Locate every blood parasite and identify its species.
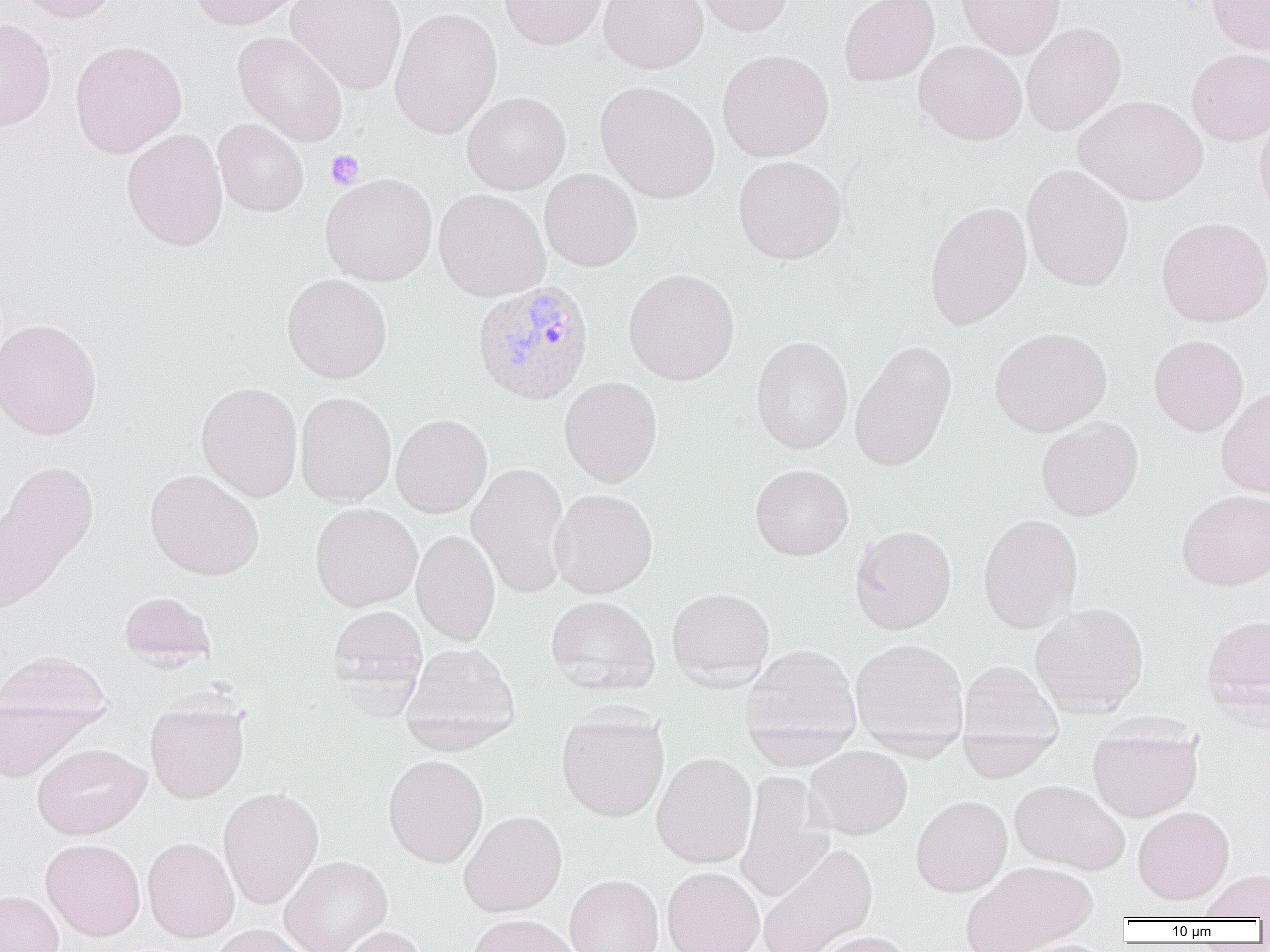

Approximate bounding boxes as [x1, y1, x2, y2] in pixels.
Plasmodium vivax-infected red blood cells: [472, 280, 594, 405].
No Plasmodium falciparum, Plasmodium ovale, Plasmodium malariae, Babesia divergens, or Trypanosoma brucei observed.

slide-level diagnosis = Plasmodium vivax
field of view = single
uninfected red blood cell locations = approximate bounding boxes as [x1, y1, x2, y2] in pixels: [10, 0, 121, 23], [188, 0, 305, 31], [286, 0, 407, 94], [498, 0, 608, 50], [598, 0, 708, 73], [692, 0, 795, 36], [839, 0, 939, 87], [956, 0, 1066, 59], [1207, 0, 1270, 56], [390, 7, 502, 139], [0, 18, 57, 132], [1021, 22, 1126, 136], [232, 31, 348, 147], [69, 39, 187, 158], [914, 40, 1027, 146], [1186, 48, 1270, 146], [716, 49, 834, 162], [595, 81, 720, 204], [462, 91, 571, 195], [1073, 95, 1206, 206], [1254, 108, 1270, 226], [213, 119, 309, 217], [121, 128, 229, 251], [733, 155, 847, 265], [1021, 164, 1134, 291], [539, 168, 642, 272], [320, 173, 437, 286], [433, 189, 550, 301], [924, 201, 1032, 330], [1156, 216, 1270, 327], [623, 268, 740, 385], [281, 274, 391, 384], [0, 318, 102, 440], [988, 327, 1112, 437], [1148, 334, 1248, 436], [751, 335, 853, 455], [849, 340, 956, 472], [559, 376, 662, 487], [195, 381, 303, 502], [1215, 385, 1270, 498], [295, 392, 396, 508], [391, 414, 492, 518], [1036, 416, 1143, 521], [1, 460, 99, 592], [467, 462, 571, 598], [750, 464, 853, 561], [145, 470, 264, 580], [549, 489, 657, 598], [1176, 489, 1270, 590], [310, 502, 422, 611], [977, 514, 1083, 634], [850, 524, 957, 634], [411, 530, 500, 646], [666, 587, 775, 689], [119, 591, 217, 669], [545, 595, 660, 695], [1029, 601, 1149, 718], [327, 605, 428, 704], [1202, 612, 1270, 719], [849, 638, 968, 751], [401, 643, 520, 752], [741, 644, 862, 758], [0, 650, 111, 727], [957, 659, 1063, 762], [0, 698, 101, 783], [145, 699, 250, 803], [556, 709, 670, 822], [1087, 721, 1203, 821], [957, 730, 1059, 783], [32, 743, 150, 839], [805, 746, 912, 839], [651, 752, 757, 869], [383, 754, 488, 867], [735, 771, 834, 903], [1009, 779, 1130, 875], [218, 786, 324, 909], [911, 795, 1012, 897], [1132, 806, 1234, 905], [458, 811, 567, 917], [142, 837, 240, 943], [40, 839, 146, 941], [757, 844, 878, 952], [279, 856, 392, 952], [961, 861, 1097, 952], [662, 866, 764, 952], [1200, 868, 1270, 920], [564, 874, 663, 952], [0, 890, 64, 952], [465, 914, 580, 952], [206, 924, 312, 952], [336, 926, 428, 952], [809, 930, 914, 952], [1001, 938, 1117, 952]
platelet locations = approximate bounding boxes as [x1, y1, x2, y2] in pixels: [325, 150, 364, 190]
preparation = thin blood film
modality = light microscopy
image size = 1270×952 pixels
magnification = 1000x